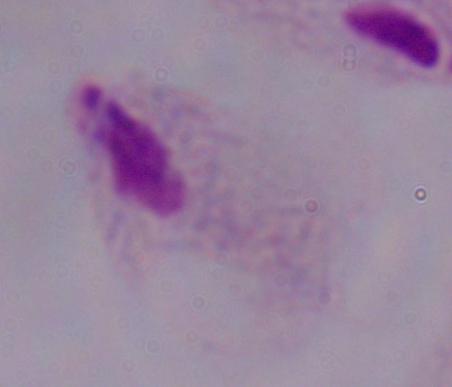

Summary:
  - Identification: trichomonad
  - Magnification: 1000x
  - Modality: micrograph